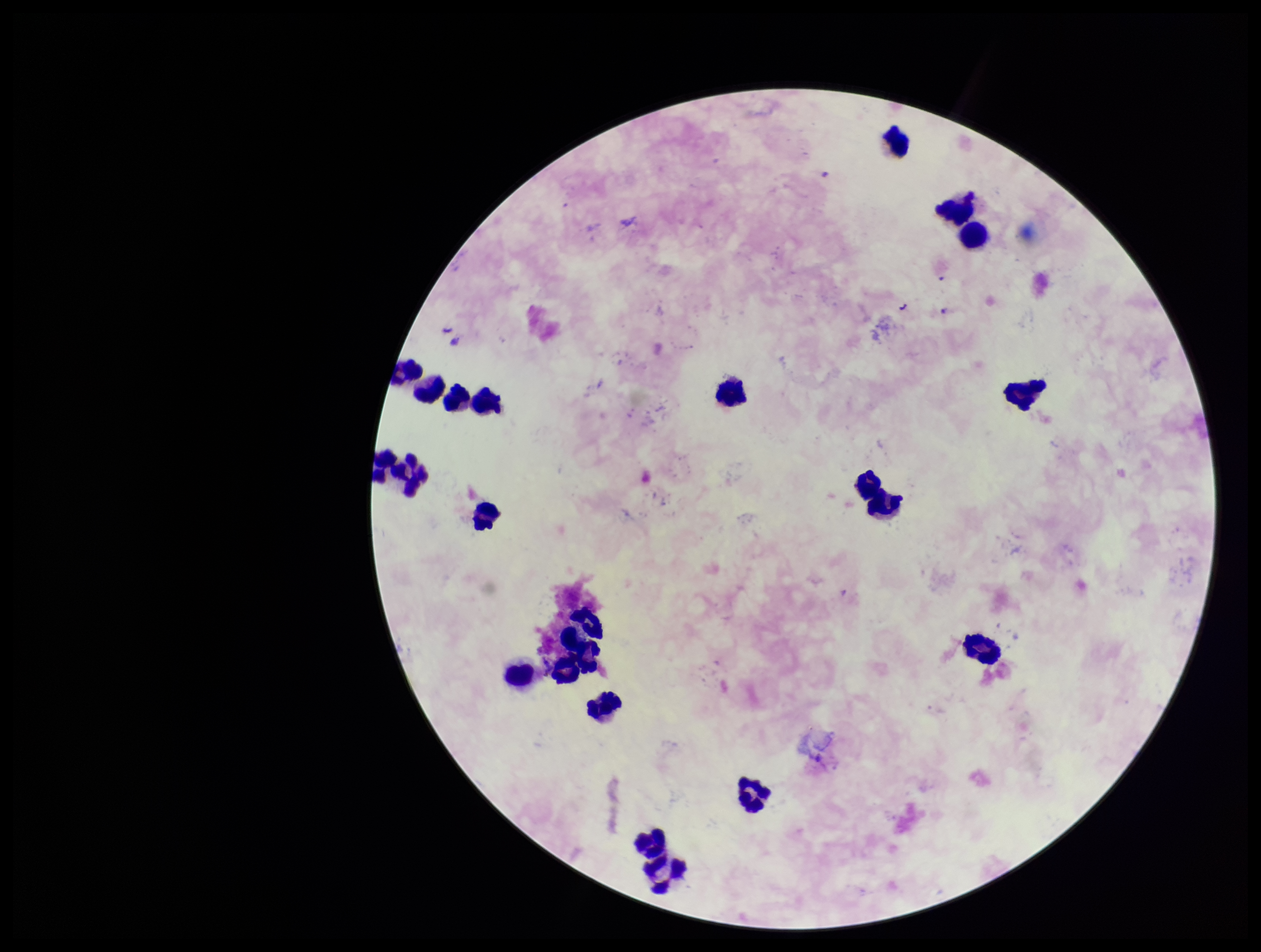
Plasmodium parasites: none detected. Stained with Giemsa. Preparation: thick smear. Image is 1261×952 pixels. Photographed through the microscope eyepiece with a smartphone camera. Patient malaria status: negative. Parasite count: 0. Leukocyte count: 23. One field from this slide.